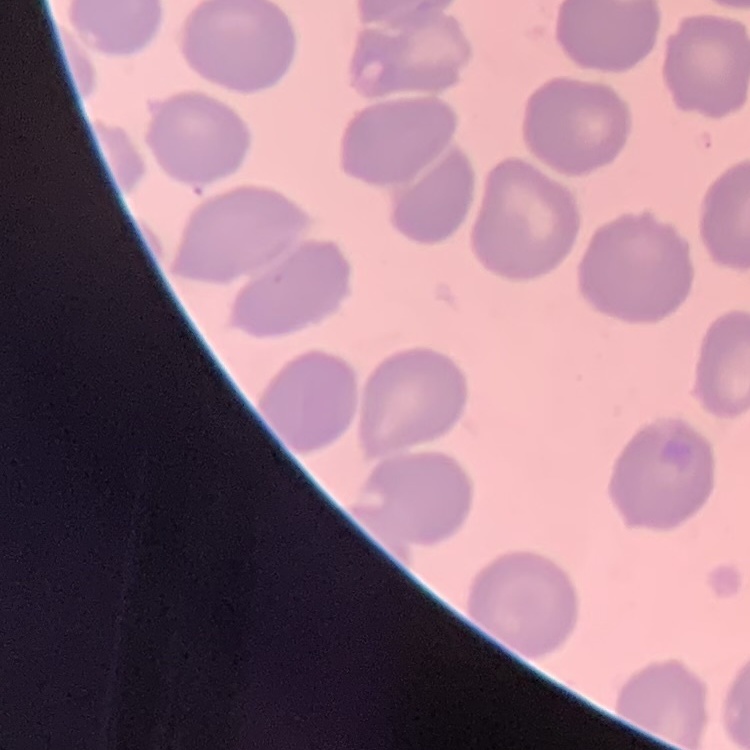
The erythrocytes exhibit no rouleaux formation. Stained with either Field's or Giemsa. Thin blood smear. Square crop of a larger photomicrograph.